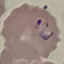
{
  "malaria_status": "parasitized",
  "stain": "Giemsa",
  "capture": "smartphone through the microscope eyepiece",
  "preparation": "thin blood smear",
  "image_type": "automatically extracted cell patch, resized to 64 × 64 pixels"
}